State the preparation type.
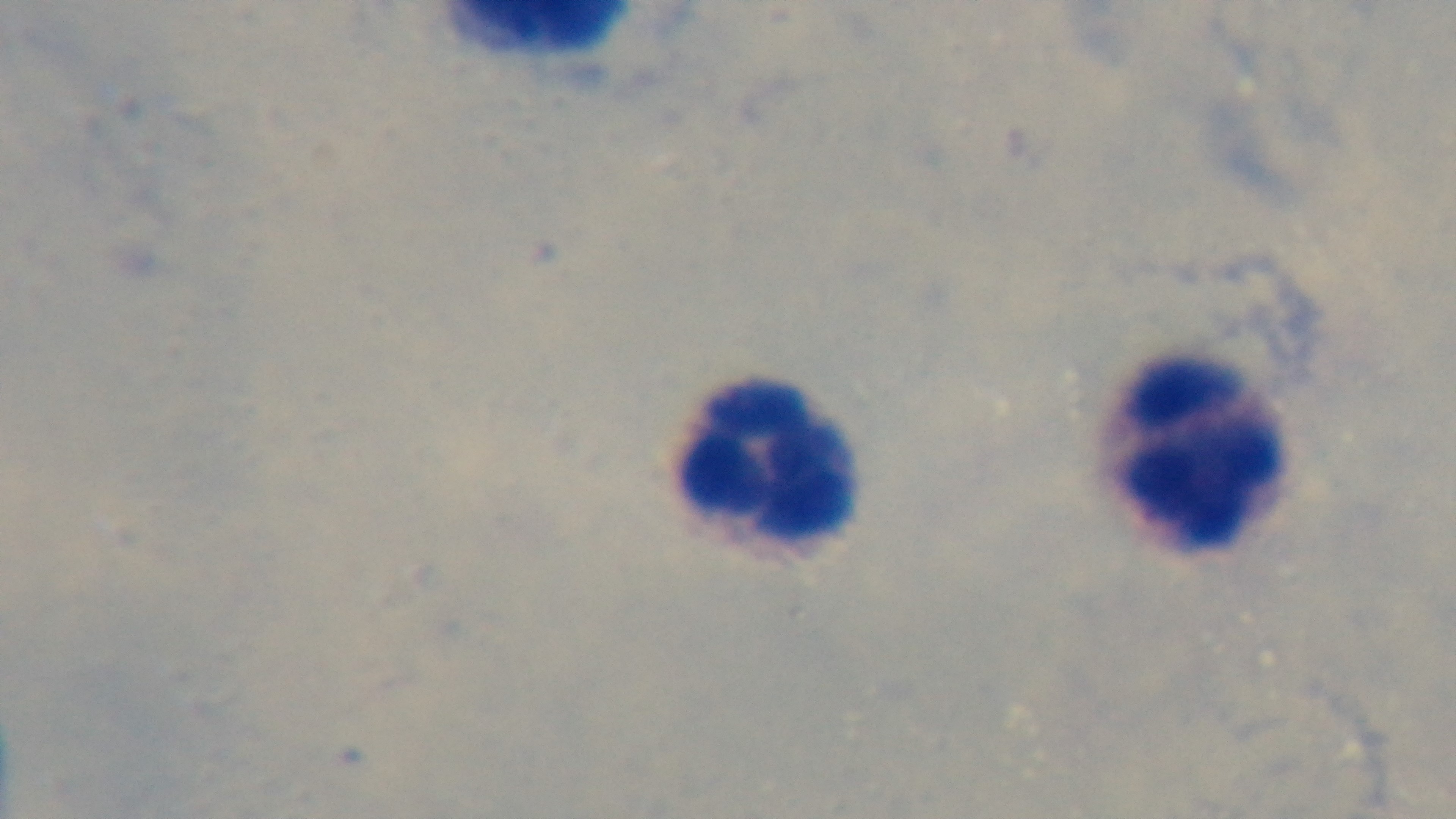
A thick smear.

Mounted 4K digital camera. Photomicrograph. One field from the slide. Oil-immersion objective, 100x. Giemsa stain. Malaria status: uninfected.